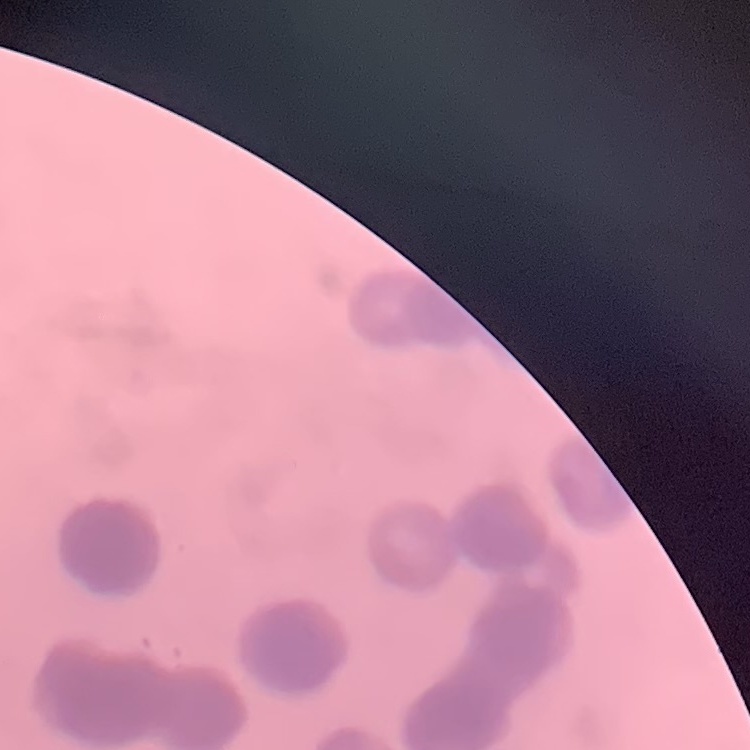

The red blood cells show rouleaux formation. Field's or Giemsa stain. One tile cut from a larger photomicrograph. Thin blood film.